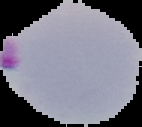
{
  "image_size": "142×127 pixels",
  "image_type": "cell region segmented out of the field of view; surrounding area masked to black",
  "preparation": "thin blood film",
  "result": "Plasmodium parasites identified"
}